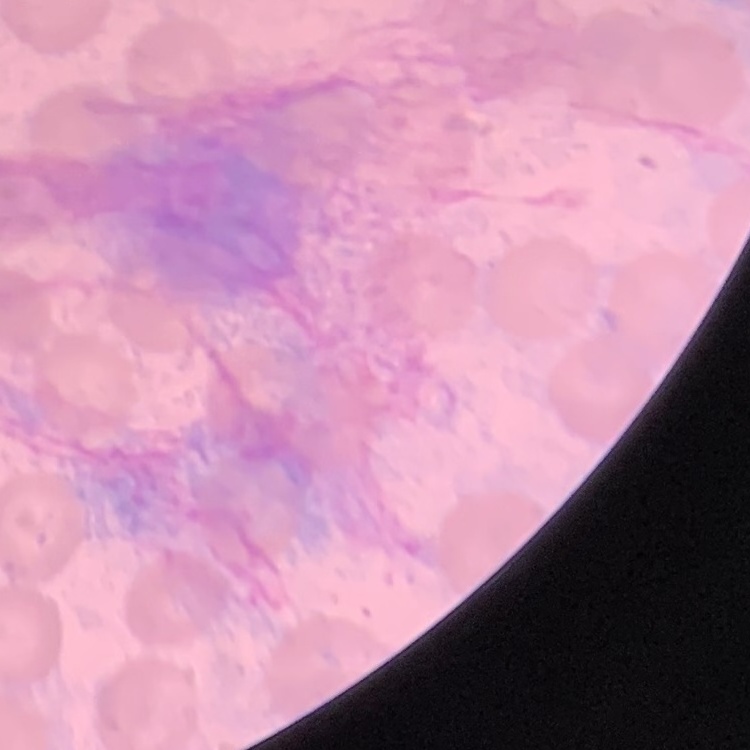 The red blood cells exhibit no rouleaux formation. Square crop of a larger photomicrograph. Stained with either Field's or Giemsa. Thin peripheral smear.